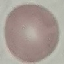

Summary:
  - Result: no malaria parasites detected
  - Preparation: thin smear
  - Capture: smartphone through the microscope eyepiece
  - Image type: cell patch, automatically extracted from a larger field of view and resized to 64 × 64 pixels
  - Stain: Giemsa